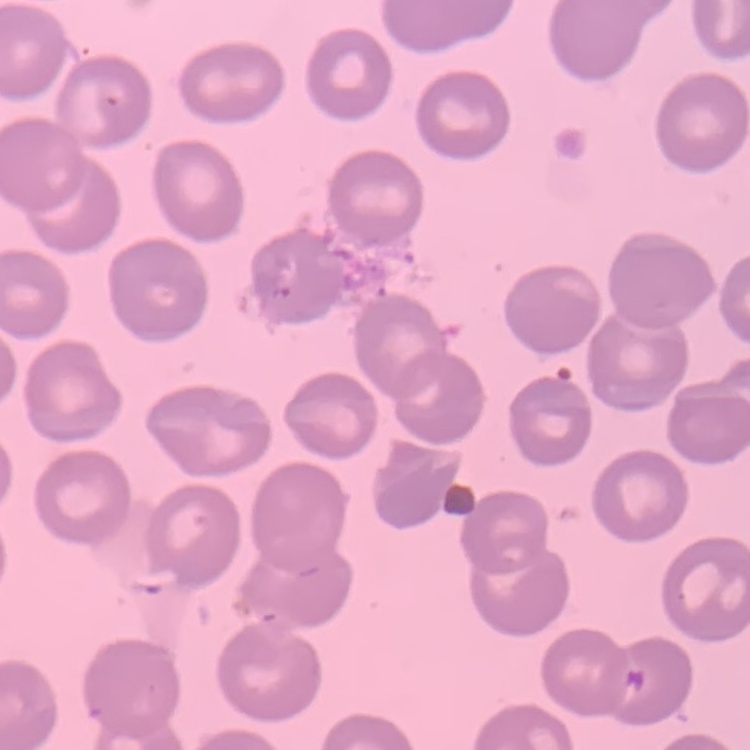

The red blood cells exhibit no rouleaux formation. Field's or Giemsa stain. One tile cut from a larger photomicrograph. Thin peripheral smear.